Report the malaria status of this cell.
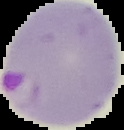
Parasitized.

Segmented cell region on a black background. Image is 124×130 pixels. From a thin blood film.